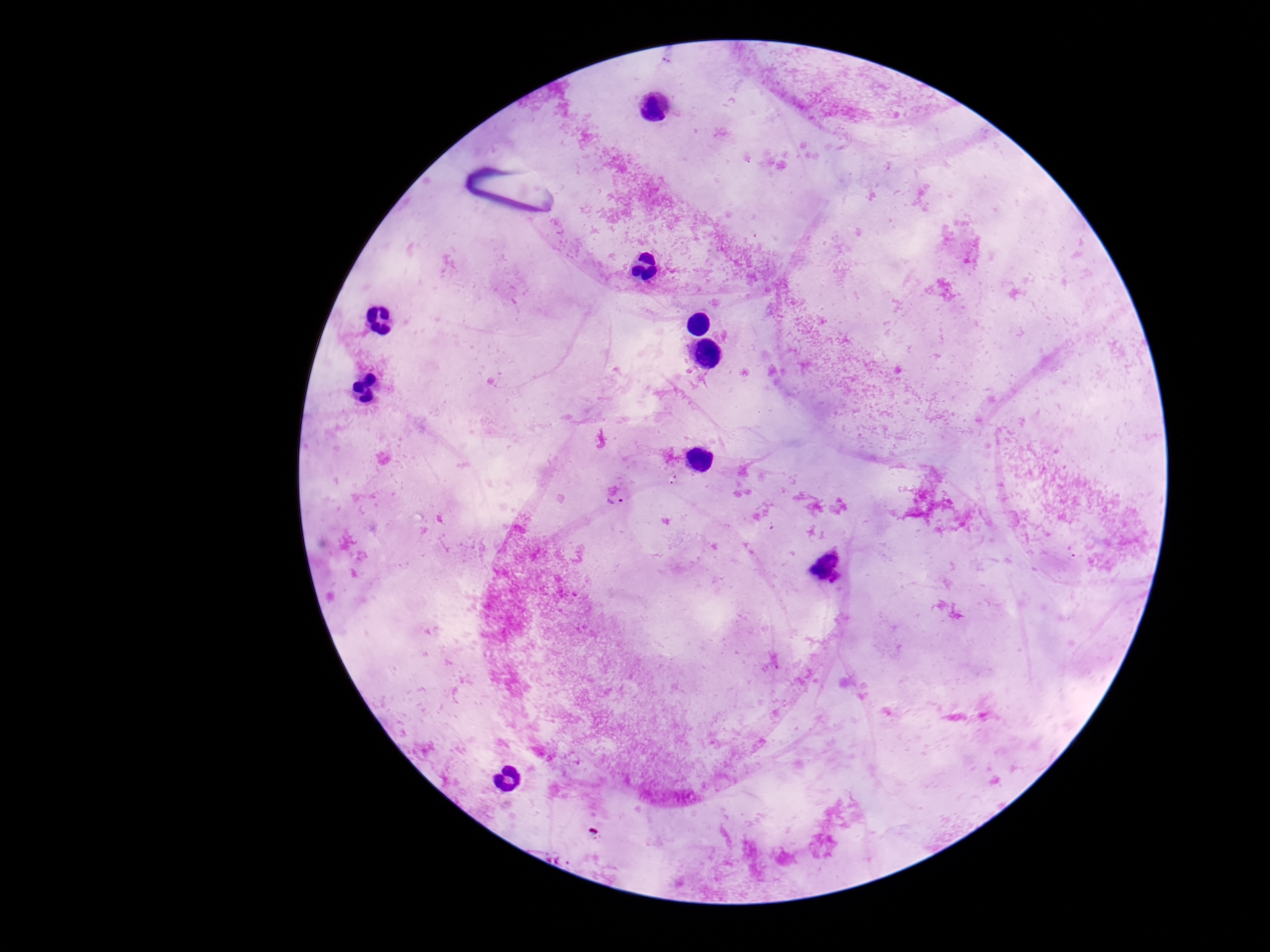
preparation: thick blood film
image_size: 1270×952 pixels
capture: smartphone camera through the microscope eyepiece
stain: Giemsa
patient_malaria_status: infected
plasmodium_parasite_locations: 'approximate centers as (x, y) in pixels: (675, 481), (615, 502), (838, 579)'
field_of_view: one from this slide
magnification: 100x